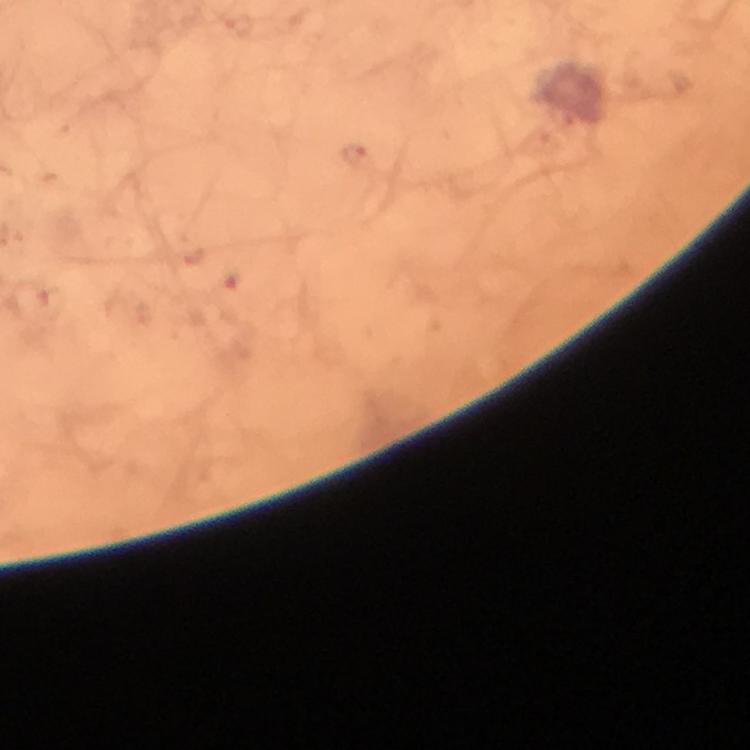
Approximate centers as (x, y) in pixels. Plasmodium parasite locations: (353, 155). Immersion oil applied. Image is 750×750 pixels. From a malaria diagnostic workup. Thick smear. Photographed through the microscope with a smartphone camera. A crop from one field of view. 100x magnification. Giemsa stain.